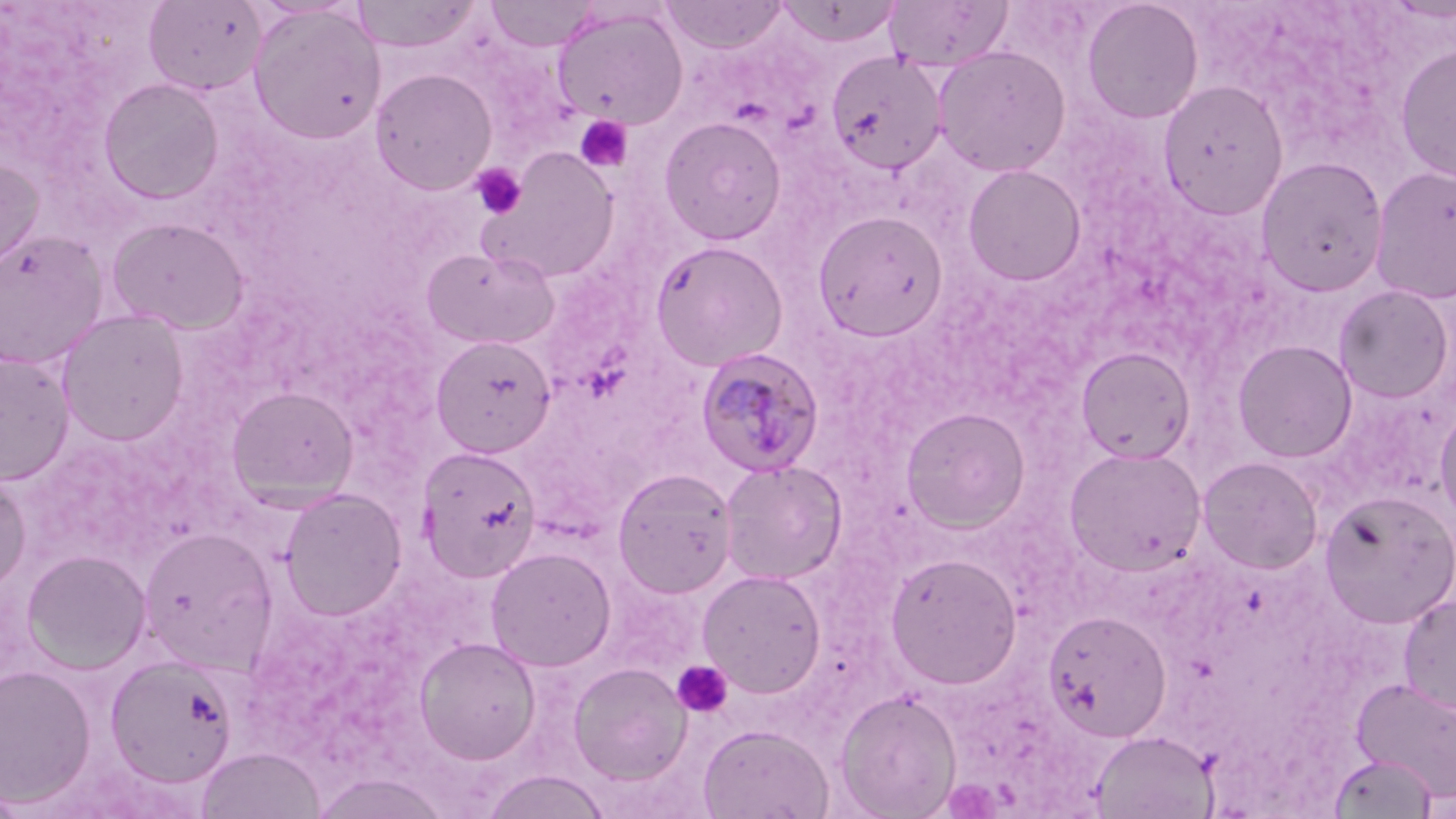

{
  "slide_level_diagnosis": "Plasmodium malariae",
  "stain": "May-Grünwald-Giemsa",
  "modality": "light microscopy",
  "field_of_view": "one of a larger specimen",
  "plasmodium_malariae_infected_red_blood_cell_locations": "approximate bounding boxes as [x1, y1, x2, y2] in pixels: [694, 348, 826, 476]",
  "preparation": "thin blood smear",
  "uninfected_red_blood_cell_locations": "approximate bounding boxes as [x1, y1, x2, y2] in pixels: [143, 0, 266, 95], [486, 0, 600, 52], [661, 0, 788, 54], [884, 0, 1013, 70], [350, 1, 481, 53], [776, 1, 903, 47], [1082, 1, 1203, 123], [248, 4, 386, 144], [552, 6, 689, 129], [1394, 41, 1456, 184], [932, 45, 1071, 177], [825, 50, 947, 175], [370, 68, 498, 194], [98, 77, 224, 204], [1158, 79, 1289, 220], [659, 115, 787, 245], [479, 147, 620, 283], [0, 156, 44, 279], [1256, 156, 1389, 297], [962, 163, 1086, 286], [1369, 165, 1456, 303], [812, 209, 949, 342], [106, 217, 250, 334], [0, 230, 108, 368], [649, 239, 790, 372], [422, 246, 560, 350], [1333, 284, 1454, 403], [56, 309, 190, 446], [430, 334, 557, 458], [1232, 339, 1358, 463], [1076, 346, 1196, 464], [0, 353, 75, 486], [226, 386, 358, 507], [1434, 402, 1456, 527], [900, 406, 1031, 533], [415, 445, 542, 582], [1063, 446, 1207, 576], [1197, 456, 1323, 574], [719, 460, 847, 585], [612, 467, 738, 598], [0, 471, 31, 595], [278, 488, 407, 620], [1319, 490, 1455, 628], [138, 526, 278, 672], [485, 546, 616, 671], [21, 549, 151, 674], [885, 552, 1022, 689], [697, 568, 827, 697], [1399, 594, 1456, 717], [1043, 610, 1172, 742], [414, 636, 541, 764], [105, 654, 239, 787], [568, 662, 692, 785], [0, 663, 97, 808], [1351, 677, 1456, 801], [834, 689, 962, 818], [697, 724, 833, 819], [1090, 730, 1218, 818], [197, 747, 326, 819], [1329, 753, 1438, 818], [480, 770, 611, 819], [309, 771, 451, 818]",
  "platelet_locations": "approximate bounding boxes as [x1, y1, x2, y2] in pixels: [574, 115, 632, 174], [471, 163, 527, 220], [671, 661, 733, 718]",
  "magnification": "1000x",
  "image_size": "1456×819 pixels"
}